Locate every Plasmodium vivax-infected red blood cell.
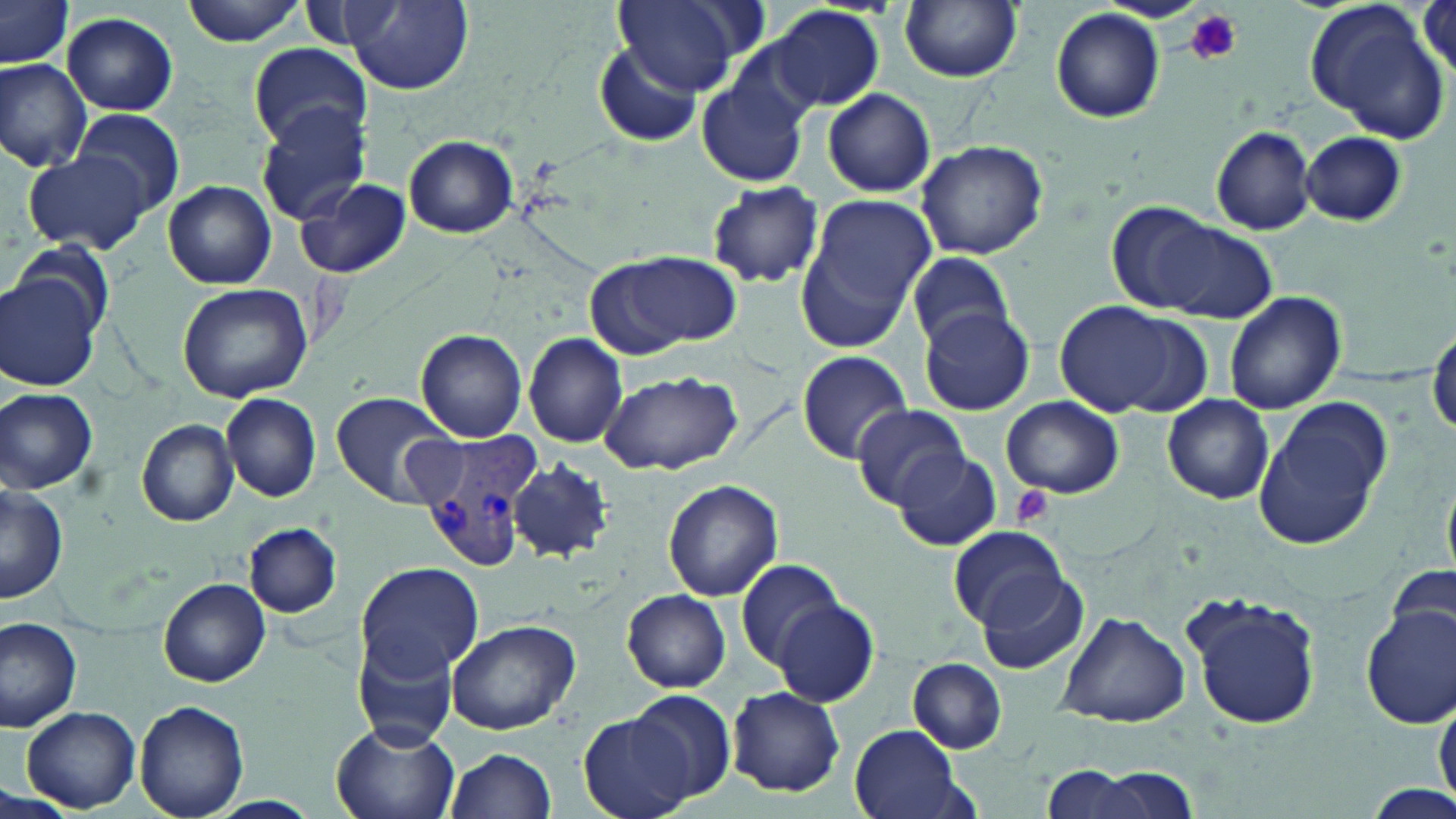

Approximate bounding boxes as (x1, y1, x2, y2) in pixels.
Plasmodium vivax-infected red blood cells: (409, 429, 541, 568).

slide-level diagnosis = Plasmodium vivax
uninfected red blood cell locations = approximate bounding boxes as (x1, y1, x2, y2) in pixels: (1, 0, 73, 68), (181, 0, 305, 46), (1305, 0, 1450, 143), (344, 1, 473, 94), (613, 2, 752, 93), (898, 2, 1025, 81), (294, 4, 409, 54), (766, 4, 884, 113), (1050, 9, 1166, 123), (61, 11, 178, 117), (2, 31, 155, 164), (595, 42, 703, 148), (249, 43, 370, 149), (0, 58, 93, 173), (696, 68, 813, 191), (824, 89, 935, 198), (256, 104, 374, 228), (75, 110, 184, 212), (1210, 125, 1317, 235), (1300, 130, 1407, 227), (404, 136, 517, 238), (915, 138, 1049, 259), (22, 148, 153, 257), (295, 177, 411, 281), (162, 180, 276, 290), (704, 180, 826, 289), (796, 196, 938, 343), (1103, 203, 1272, 321), (12, 244, 117, 336), (605, 251, 742, 351), (905, 253, 1015, 348), (1, 271, 103, 392), (177, 282, 314, 403), (1223, 291, 1345, 415), (1053, 302, 1196, 418), (918, 307, 1034, 416), (1429, 327, 1456, 439), (415, 329, 528, 442), (523, 333, 628, 448), (797, 351, 912, 463), (599, 370, 742, 476), (0, 388, 98, 493), (330, 390, 457, 506), (222, 393, 320, 502), (1161, 395, 1274, 505), (1000, 396, 1125, 500), (1252, 399, 1392, 553), (849, 404, 971, 510), (137, 419, 239, 526), (893, 448, 1003, 551), (508, 457, 616, 563), (663, 479, 783, 601), (1, 484, 69, 602), (245, 523, 340, 617), (948, 524, 1066, 627), (736, 557, 845, 670), (354, 560, 482, 680), (1384, 562, 1455, 656), (977, 573, 1087, 677), (159, 578, 271, 687), (624, 590, 730, 691), (1185, 593, 1322, 731), (773, 600, 878, 706), (1361, 608, 1456, 729), (1055, 610, 1191, 727), (0, 617, 82, 730), (444, 618, 581, 736), (353, 629, 462, 749), (907, 658, 1007, 754), (877, 670, 998, 804), (727, 687, 845, 796), (625, 691, 737, 807), (1434, 697, 1456, 805), (133, 701, 249, 819), (21, 707, 139, 813), (578, 713, 694, 819), (329, 718, 460, 819), (848, 725, 966, 819), (444, 748, 557, 819), (1042, 765, 1142, 819), (1074, 767, 1203, 818)
platelet locations = approximate bounding boxes as (x1, y1, x2, y2) in pixels: (1186, 9, 1241, 65), (1012, 485, 1055, 527)
field of view = single
magnification = 1000x
modality = light microscopy
image size = 1456×819 pixels
stain = May-Grünwald-Giemsa
preparation = thin blood smear